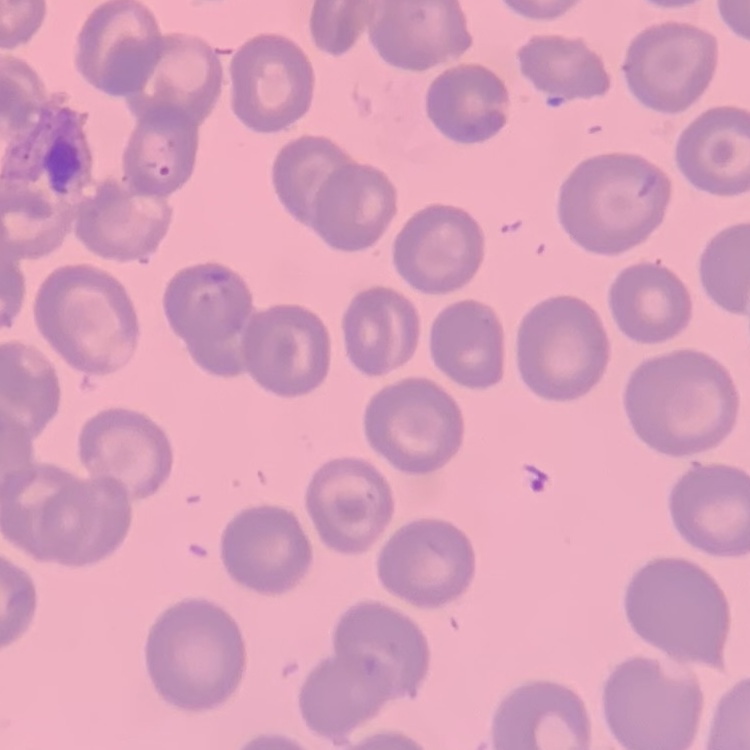 The erythrocytes exhibit no rouleaux formation. Thin peripheral smear. Square crop of a larger photomicrograph. Stained with either Field's or Giemsa.